Comment on the morphology of the erythrocytes.
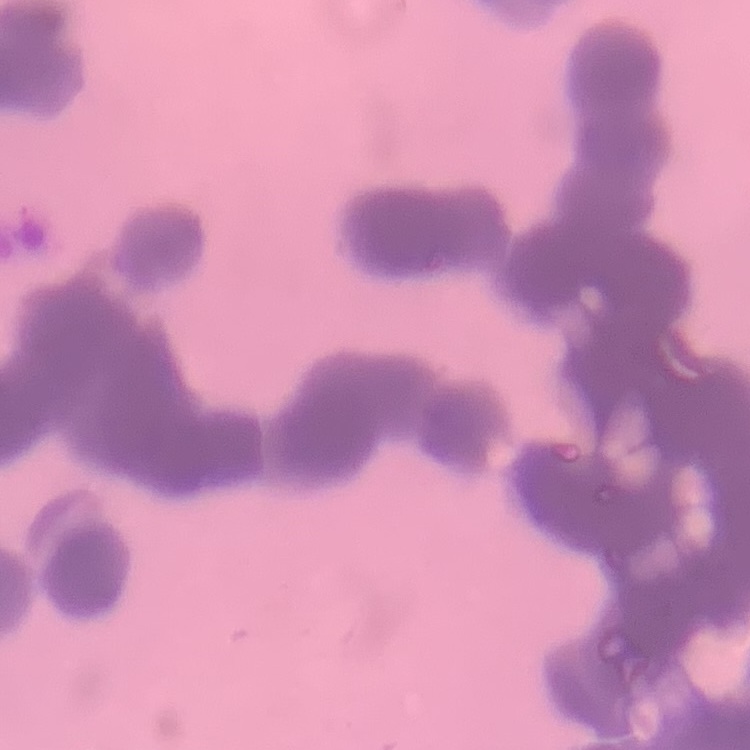
They show rouleaux formation.

Thin blood film. Field's or Giemsa stain. One tile cut from a larger photomicrograph.